State which parasite is depicted.
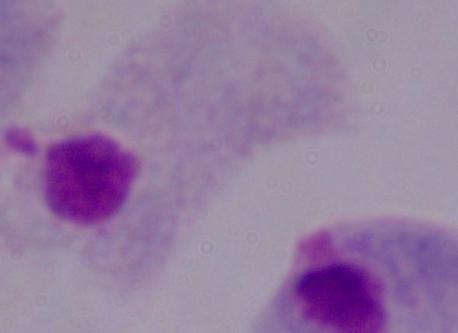

This is a trichomonad.

modality = photomicrograph
magnification = 1000x